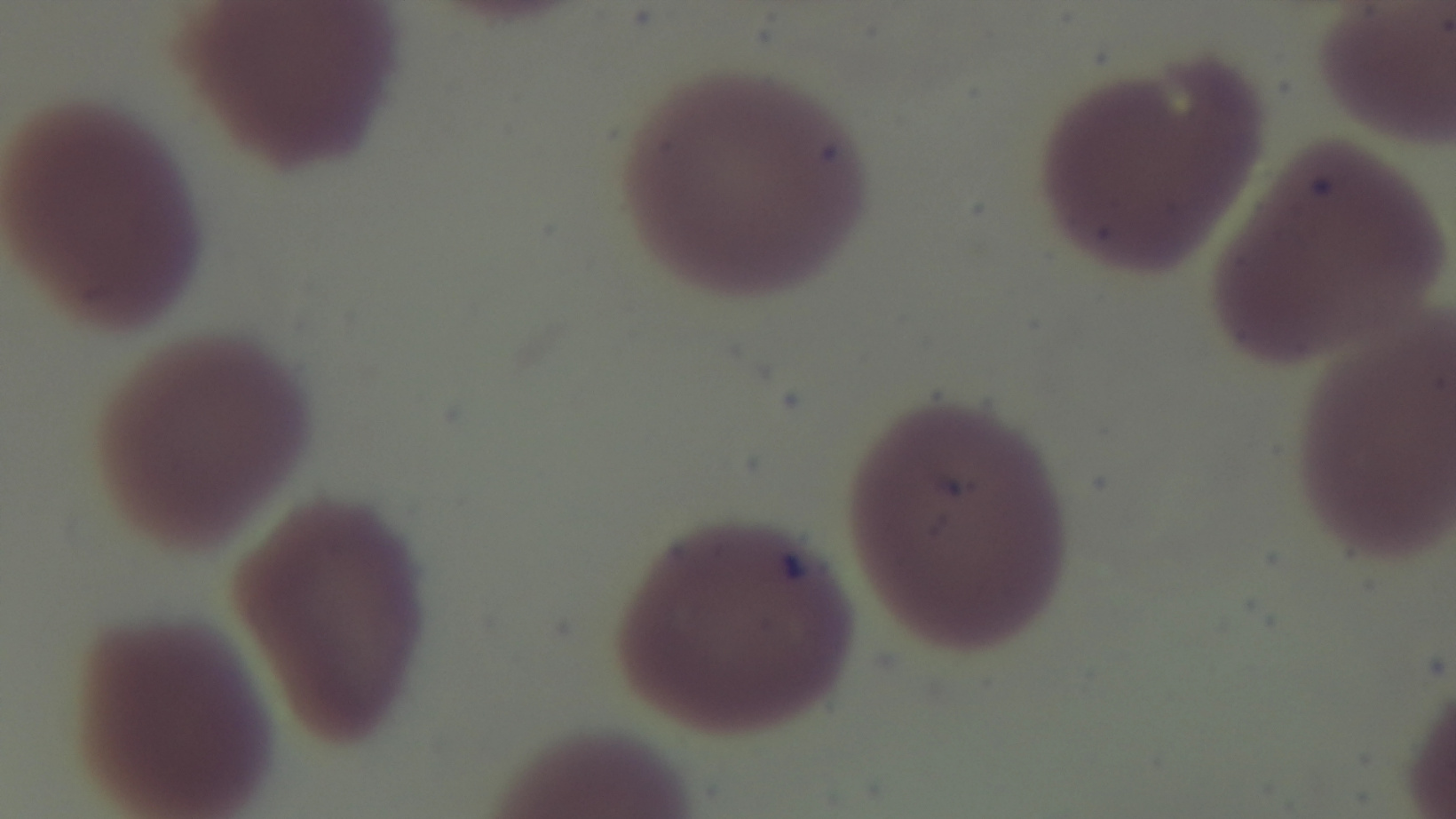
Summary:
  - Malaria status: uninfected
  - Stain: Giemsa
  - Field of view: one from the slide
  - Objective: 100x oil immersion
  - Modality: light microscopy
  - Preparation: thin smear
  - Capture: mounted 4K digital camera